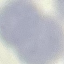
Malaria status: uninfected. Thin smear of blood. Giemsa-stained preparation. Automatically extracted cell patch, resized to 64 × 64 pixels. Acquired by smartphone through the microscope eyepiece.